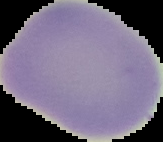
Result: negative for Plasmodium parasites. From a thin blood smear. Image is 163×142 pixels. Cell region segmented out of the field of view; the surrounding area is masked to black.